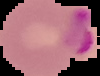

image type = segmented cell region on a black background
malaria status = parasitized
image size = 100×76 pixels
preparation = thin blood film